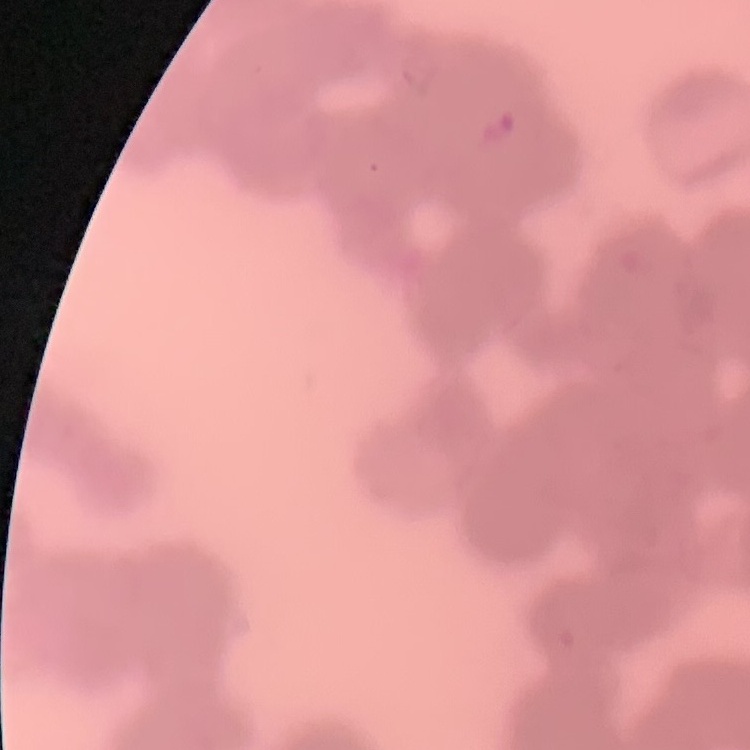

{
  "red_blood_cell_morphology": "rouleaux formation",
  "stain": "Field's or Giemsa",
  "preparation": "thin blood smear",
  "image_type": "square crop of a larger photomicrograph"
}